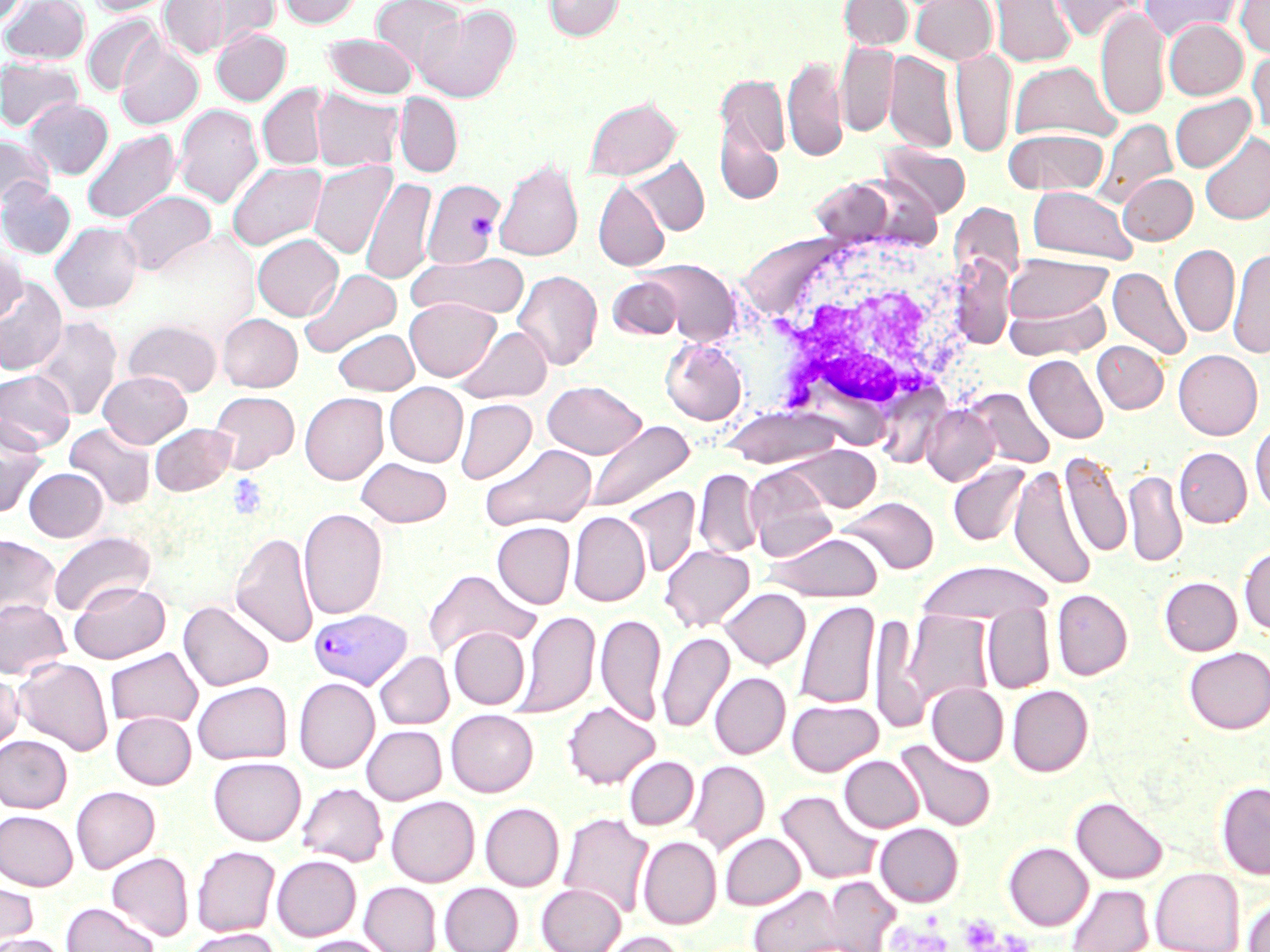 Approximate bounding boxes as named x1/y1/x2/y2 corners in pixels. Platelet locations: (x1=227, y1=474, x2=269, y2=521), (x1=957, y1=915, x2=1003, y2=951). White blood cell locations: (x1=741, y1=226, x2=979, y2=430). Plasmodium vivax-infected red blood cell locations: (x1=309, y1=608, x2=413, y2=690). Uninfected red blood cell locations: (x1=0, y1=0, x2=28, y2=27), (x1=1, y1=0, x2=90, y2=64), (x1=87, y1=0, x2=178, y2=16), (x1=184, y1=0, x2=280, y2=51), (x1=278, y1=0, x2=362, y2=28), (x1=371, y1=0, x2=467, y2=75), (x1=543, y1=0, x2=623, y2=40), (x1=839, y1=0, x2=913, y2=50), (x1=911, y1=0, x2=997, y2=64), (x1=990, y1=0, x2=1075, y2=67), (x1=1047, y1=0, x2=1141, y2=41), (x1=1141, y1=0, x2=1241, y2=42), (x1=1236, y1=0, x2=1270, y2=57), (x1=160, y1=1, x2=233, y2=60), (x1=1095, y1=5, x2=1169, y2=121), (x1=414, y1=6, x2=519, y2=103), (x1=82, y1=14, x2=164, y2=97), (x1=1164, y1=20, x2=1247, y2=99), (x1=212, y1=28, x2=291, y2=105), (x1=323, y1=34, x2=417, y2=98), (x1=116, y1=37, x2=203, y2=129), (x1=836, y1=41, x2=898, y2=137), (x1=950, y1=48, x2=1016, y2=157), (x1=1247, y1=48, x2=1270, y2=135), (x1=884, y1=50, x2=957, y2=153), (x1=783, y1=54, x2=846, y2=161), (x1=0, y1=57, x2=84, y2=132), (x1=1008, y1=61, x2=1120, y2=143), (x1=715, y1=72, x2=790, y2=185), (x1=258, y1=84, x2=327, y2=170), (x1=310, y1=88, x2=404, y2=172), (x1=395, y1=93, x2=462, y2=177), (x1=1170, y1=94, x2=1255, y2=172), (x1=584, y1=96, x2=681, y2=181), (x1=24, y1=98, x2=113, y2=179), (x1=174, y1=104, x2=263, y2=208), (x1=1094, y1=119, x2=1177, y2=207), (x1=81, y1=128, x2=181, y2=224), (x1=1004, y1=128, x2=1108, y2=195), (x1=1199, y1=132, x2=1270, y2=225), (x1=0, y1=134, x2=55, y2=209), (x1=879, y1=144, x2=971, y2=218), (x1=628, y1=157, x2=709, y2=235), (x1=494, y1=158, x2=583, y2=262), (x1=308, y1=159, x2=397, y2=259), (x1=227, y1=161, x2=326, y2=250), (x1=1118, y1=173, x2=1197, y2=244), (x1=361, y1=176, x2=436, y2=286), (x1=422, y1=179, x2=504, y2=268), (x1=0, y1=180, x2=76, y2=259), (x1=593, y1=180, x2=670, y2=271), (x1=1027, y1=186, x2=1137, y2=264), (x1=119, y1=190, x2=215, y2=275), (x1=949, y1=201, x2=1025, y2=287), (x1=50, y1=222, x2=142, y2=313), (x1=253, y1=234, x2=342, y2=320), (x1=1169, y1=244, x2=1240, y2=337), (x1=0, y1=247, x2=25, y2=324), (x1=1228, y1=248, x2=1270, y2=358), (x1=408, y1=253, x2=531, y2=320), (x1=1005, y1=253, x2=1112, y2=326), (x1=638, y1=258, x2=741, y2=345), (x1=950, y1=260, x2=1015, y2=348), (x1=1108, y1=266, x2=1191, y2=361), (x1=299, y1=268, x2=402, y2=358), (x1=513, y1=270, x2=603, y2=371), (x1=0, y1=276, x2=67, y2=376), (x1=607, y1=276, x2=684, y2=339), (x1=1004, y1=291, x2=1111, y2=361), (x1=405, y1=297, x2=499, y2=381), (x1=217, y1=313, x2=302, y2=392), (x1=29, y1=316, x2=122, y2=420), (x1=124, y1=319, x2=222, y2=397), (x1=455, y1=325, x2=553, y2=403), (x1=333, y1=328, x2=419, y2=395), (x1=660, y1=339, x2=747, y2=425), (x1=1093, y1=341, x2=1168, y2=413), (x1=1173, y1=349, x2=1263, y2=439), (x1=1025, y1=354, x2=1108, y2=445), (x1=0, y1=370, x2=75, y2=452), (x1=98, y1=370, x2=192, y2=447), (x1=542, y1=380, x2=646, y2=459), (x1=385, y1=382, x2=468, y2=467), (x1=966, y1=388, x2=1055, y2=470), (x1=209, y1=391, x2=299, y2=472), (x1=300, y1=392, x2=388, y2=484), (x1=455, y1=398, x2=536, y2=484), (x1=921, y1=403, x2=1001, y2=486), (x1=721, y1=406, x2=845, y2=469), (x1=0, y1=418, x2=49, y2=517), (x1=584, y1=419, x2=695, y2=514), (x1=1250, y1=421, x2=1270, y2=513), (x1=64, y1=423, x2=156, y2=510), (x1=150, y1=423, x2=236, y2=496), (x1=480, y1=443, x2=597, y2=532), (x1=785, y1=444, x2=881, y2=512), (x1=1174, y1=447, x2=1251, y2=527), (x1=1059, y1=451, x2=1131, y2=560), (x1=357, y1=458, x2=452, y2=527), (x1=948, y1=462, x2=1030, y2=546), (x1=744, y1=465, x2=837, y2=559), (x1=1009, y1=466, x2=1096, y2=591), (x1=24, y1=467, x2=108, y2=541), (x1=694, y1=469, x2=763, y2=559), (x1=1123, y1=469, x2=1187, y2=568), (x1=622, y1=485, x2=701, y2=577), (x1=839, y1=496, x2=939, y2=574), (x1=298, y1=508, x2=387, y2=620), (x1=569, y1=511, x2=650, y2=606), (x1=492, y1=522, x2=575, y2=608), (x1=48, y1=531, x2=155, y2=616), (x1=230, y1=531, x2=319, y2=648), (x1=765, y1=532, x2=883, y2=602), (x1=0, y1=535, x2=61, y2=621), (x1=660, y1=544, x2=755, y2=632), (x1=1239, y1=544, x2=1270, y2=636), (x1=915, y1=561, x2=1054, y2=624), (x1=423, y1=569, x2=539, y2=658), (x1=1160, y1=577, x2=1241, y2=655), (x1=70, y1=581, x2=170, y2=663), (x1=720, y1=587, x2=810, y2=669), (x1=1052, y1=589, x2=1132, y2=680), (x1=0, y1=599, x2=70, y2=679), (x1=795, y1=600, x2=880, y2=710), (x1=178, y1=601, x2=274, y2=690), (x1=983, y1=603, x2=1054, y2=693), (x1=514, y1=610, x2=600, y2=718), (x1=901, y1=610, x2=993, y2=710), (x1=596, y1=613, x2=666, y2=726), (x1=868, y1=614, x2=925, y2=733), (x1=449, y1=627, x2=530, y2=709), (x1=657, y1=631, x2=734, y2=733), (x1=1184, y1=646, x2=1270, y2=734), (x1=105, y1=647, x2=202, y2=728), (x1=375, y1=651, x2=453, y2=729), (x1=14, y1=657, x2=114, y2=755), (x1=0, y1=671, x2=24, y2=752), (x1=710, y1=672, x2=790, y2=758), (x1=294, y1=677, x2=379, y2=773), (x1=193, y1=680, x2=292, y2=764), (x1=927, y1=683, x2=1009, y2=765), (x1=1007, y1=685, x2=1093, y2=775), (x1=787, y1=699, x2=883, y2=776), (x1=563, y1=701, x2=659, y2=789), (x1=445, y1=709, x2=538, y2=796), (x1=111, y1=712, x2=196, y2=789), (x1=362, y1=725, x2=446, y2=804), (x1=0, y1=735, x2=71, y2=812), (x1=895, y1=739, x2=996, y2=831), (x1=839, y1=755, x2=923, y2=832), (x1=624, y1=756, x2=699, y2=830), (x1=208, y1=757, x2=306, y2=845), (x1=686, y1=760, x2=769, y2=855), (x1=298, y1=782, x2=388, y2=866), (x1=1216, y1=782, x2=1270, y2=878), (x1=71, y1=786, x2=160, y2=873), (x1=775, y1=789, x2=882, y2=886), (x1=386, y1=795, x2=479, y2=887), (x1=1071, y1=796, x2=1167, y2=883), (x1=480, y1=802, x2=564, y2=891), (x1=0, y1=810, x2=78, y2=890), (x1=558, y1=812, x2=654, y2=919), (x1=875, y1=823, x2=963, y2=907), (x1=720, y1=832, x2=805, y2=909), (x1=638, y1=836, x2=721, y2=929), (x1=1004, y1=842, x2=1093, y2=930), (x1=192, y1=845, x2=280, y2=936), (x1=107, y1=852, x2=193, y2=941), (x1=272, y1=855, x2=361, y2=940), (x1=1150, y1=867, x2=1244, y2=952), (x1=823, y1=877, x2=900, y2=951), (x1=0, y1=878, x2=39, y2=948), (x1=360, y1=881, x2=441, y2=952), (x1=439, y1=882, x2=523, y2=952), (x1=537, y1=883, x2=625, y2=952), (x1=1066, y1=883, x2=1153, y2=952), (x1=749, y1=885, x2=846, y2=952), (x1=1243, y1=897, x2=1270, y2=952), (x1=61, y1=902, x2=160, y2=952), (x1=183, y1=927, x2=282, y2=952), (x1=600, y1=930, x2=689, y2=952), (x1=0, y1=934, x2=69, y2=952), (x1=298, y1=935, x2=392, y2=952). Slide-level diagnosis: Plasmodium vivax. Image is 1270×952 pixels. Thin blood smear. Light microscopy. One field of a larger specimen. May-Grünwald-Giemsa stain. Captured at 1000x magnification.